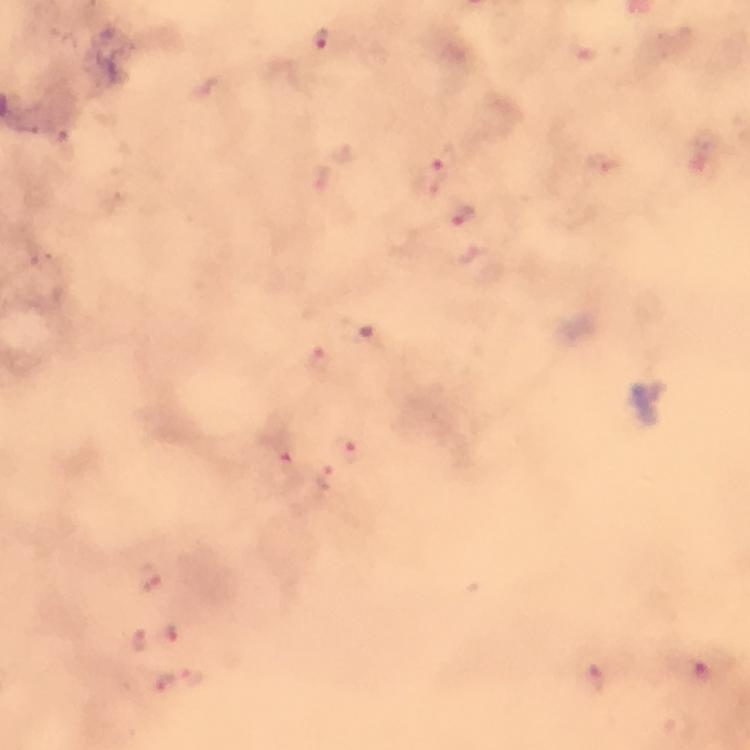

context = from a diagnostic examination for malaria
preparation = thick smear
immersion oil = used
magnification = 100x
capture = smartphone photograph through a microscope
stain = Giemsa
cropped from = one field of view
image size = 750×750 pixels
malaria parasite locations = approximate centers as (x, y) in pixels: (320, 40), (445, 162), (465, 220), (317, 358), (348, 450), (286, 458), (154, 579), (172, 633), (141, 642), (192, 677), (590, 680), (165, 683)